Evaluate for Plasmodium parasites.
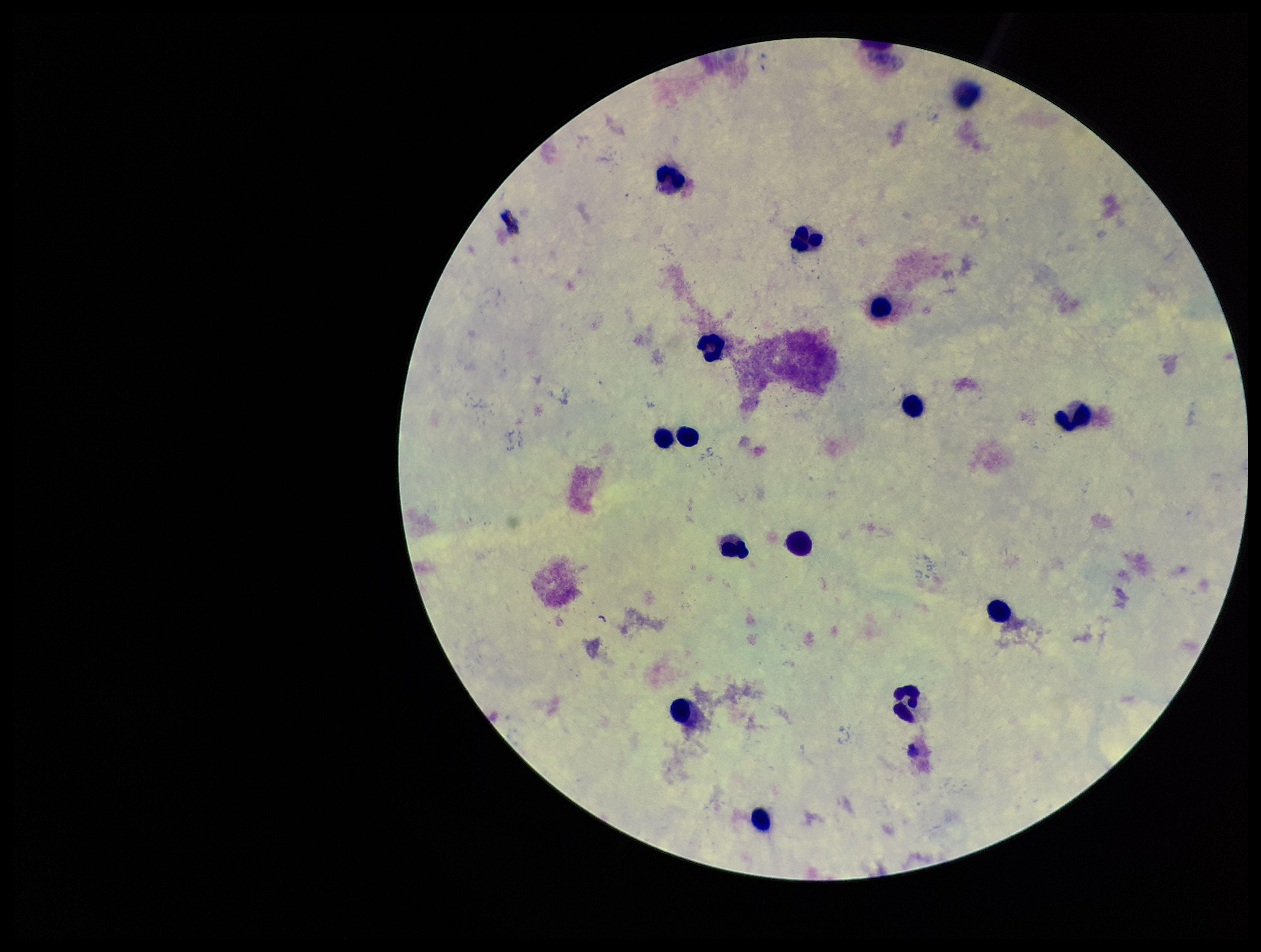

None identified.

Summary:
  - Preparation: thick smear
  - Patient malaria status: negative
  - Field of view: single
  - Image size: 1261×952 pixels
  - Capture: smartphone photograph through the microscope eyepiece
  - Leukocyte count: 15
  - Stain: Giemsa
  - Parasite count: 0